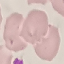
malaria_status: uninfected
image_type: cell patch, automatically extracted from a larger field of view and resized to 64 × 64 pixels
preparation: thin smear
stain: Giemsa
capture: smartphone through the microscope eyepiece